Locate every uninfected red blood cell.
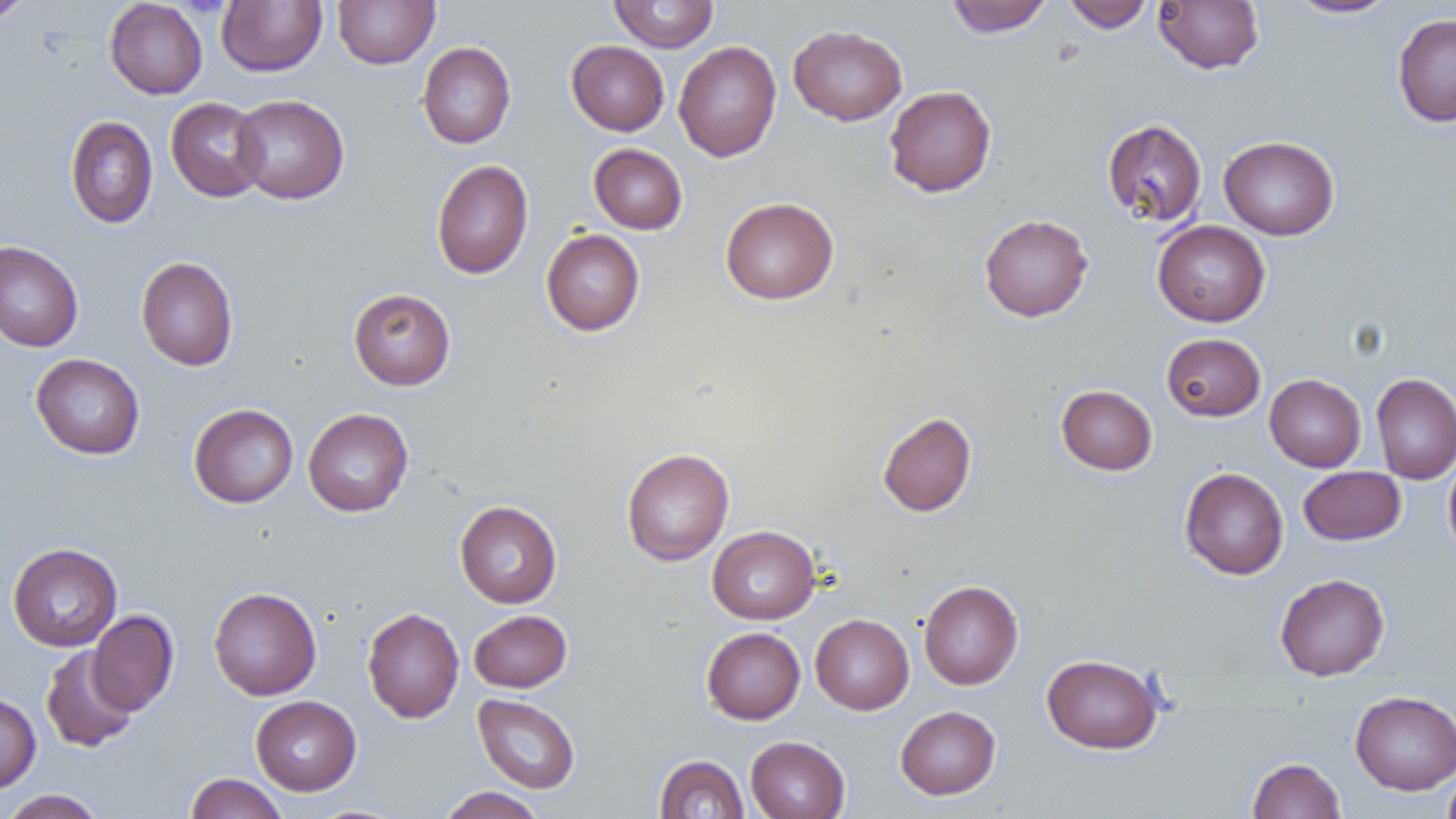

Approximate bounding boxes as (x1, y1, x2, y2) in pixels.
Uninfected red blood cells: (0, 0, 34, 27), (332, 0, 440, 69), (608, 0, 719, 52), (945, 0, 1053, 37), (1063, 0, 1155, 33), (1153, 0, 1264, 74), (1286, 0, 1398, 19), (104, 1, 208, 99), (216, 1, 327, 76), (1392, 13, 1456, 127), (788, 24, 907, 126), (566, 40, 669, 136), (673, 41, 782, 162), (418, 42, 516, 148), (884, 85, 997, 197), (231, 94, 350, 204), (166, 97, 268, 202), (65, 115, 158, 227), (1101, 118, 1207, 228), (1218, 135, 1340, 240), (588, 143, 687, 235), (431, 159, 533, 279), (720, 196, 839, 304), (979, 214, 1093, 322), (1152, 220, 1270, 326), (541, 229, 645, 336), (0, 240, 84, 353), (136, 256, 239, 371), (348, 288, 456, 390), (1161, 333, 1266, 421), (30, 353, 145, 459), (1371, 372, 1456, 484), (1265, 374, 1366, 472), (1056, 385, 1157, 476), (188, 403, 299, 508), (303, 408, 414, 517), (877, 411, 977, 517), (621, 448, 734, 566), (1444, 454, 1456, 560), (1298, 466, 1406, 545), (1179, 467, 1289, 580), (455, 500, 562, 608), (707, 525, 820, 624), (7, 542, 122, 651), (1275, 573, 1390, 681), (918, 580, 1023, 690), (208, 587, 322, 700), (362, 607, 464, 723), (88, 610, 179, 716), (469, 610, 572, 692), (810, 614, 914, 715), (701, 627, 805, 724), (40, 646, 138, 753), (1041, 653, 1164, 754), (1350, 691, 1456, 794), (0, 692, 41, 793), (473, 693, 581, 793), (250, 695, 361, 795), (895, 705, 1001, 800), (745, 735, 850, 819), (654, 754, 749, 818), (1247, 757, 1345, 818), (1442, 767, 1456, 819), (185, 773, 288, 819), (438, 786, 546, 819), (1, 789, 106, 819).

slide-level diagnosis = negative for blood parasites
field of view = one of a larger specimen
image size = 1456×819 pixels
modality = optical microscopy
preparation = thin blood smear
magnification = 1000x